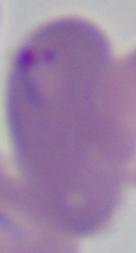

Summary:
  - Identification: Babesia
  - Magnification: 1000x
  - Modality: micrograph